Classify this cell by malaria status.
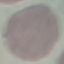
Uninfected.

Thin blood film. Automatically extracted cell patch, resized to 64 × 64 pixels. Giemsa stain. Photographed with a smartphone camera at the microscope eyepiece.